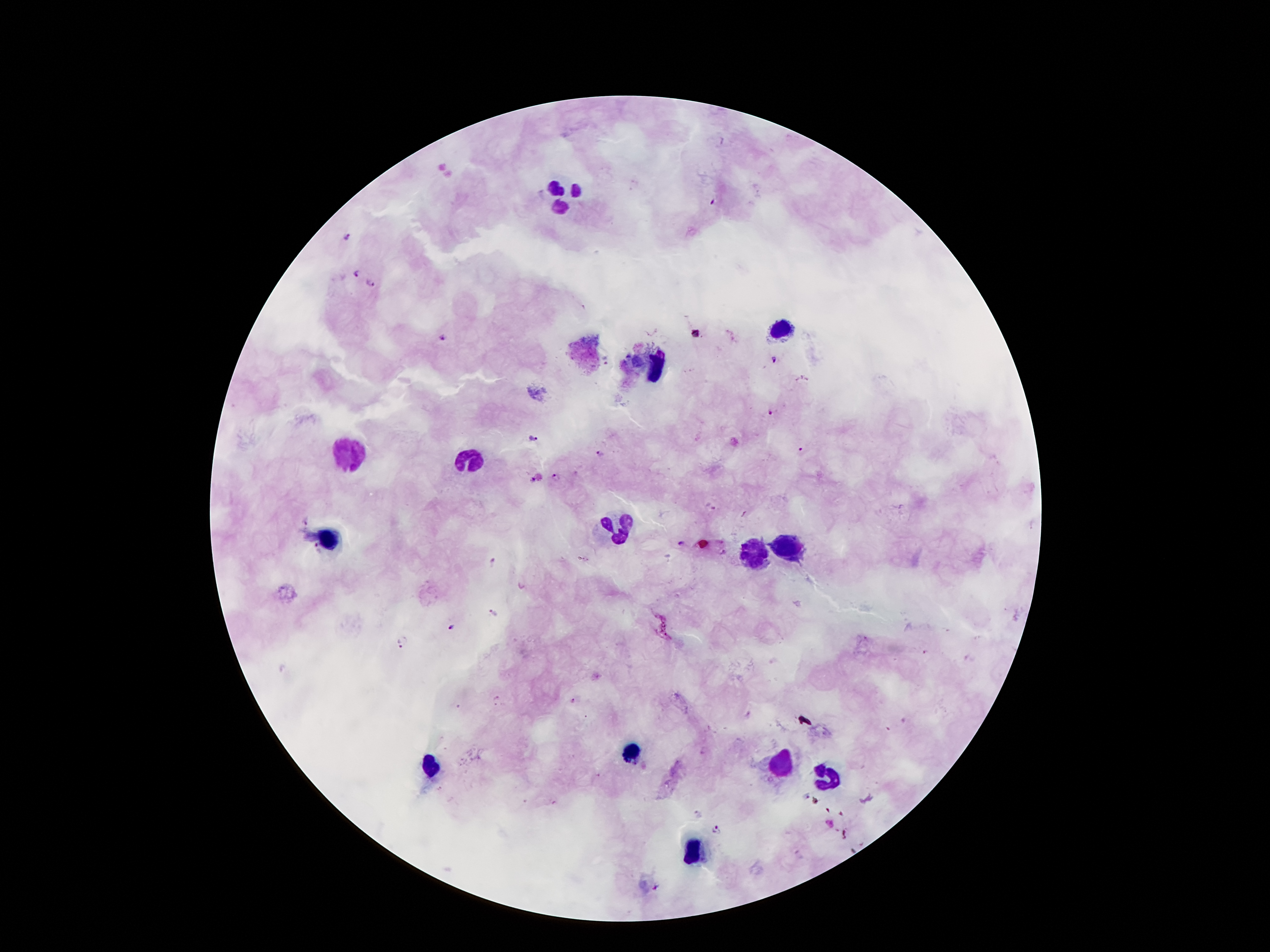
patient_malaria_status: infected with Plasmodium falciparum
stain: Giemsa
preparation: thick blood smear
malaria_parasite_locations: 'approximate centers as [x, y] in pixels: [713, 204], [348, 235], [354, 272], [371, 284], [442, 337], [775, 360], [769, 411], [534, 437], [802, 451], [599, 453], [557, 478], [529, 480], [306, 520], [681, 543], [316, 548], [495, 562], [490, 611], [453, 628], [400, 643], [696, 814], [716, 829], [656, 888]'
leukocyte_locations: 'approximate centers as [x, y] in pixels: [566, 197], [779, 329], [658, 369], [346, 453], [471, 458], [615, 530], [330, 539], [788, 549], [747, 552], [633, 754], [778, 766], [429, 768], [826, 776], [691, 850]'
capture: smartphone through the microscope eyepiece
field_of_view: single
image_size: 1270×952 pixels
magnification: 100x